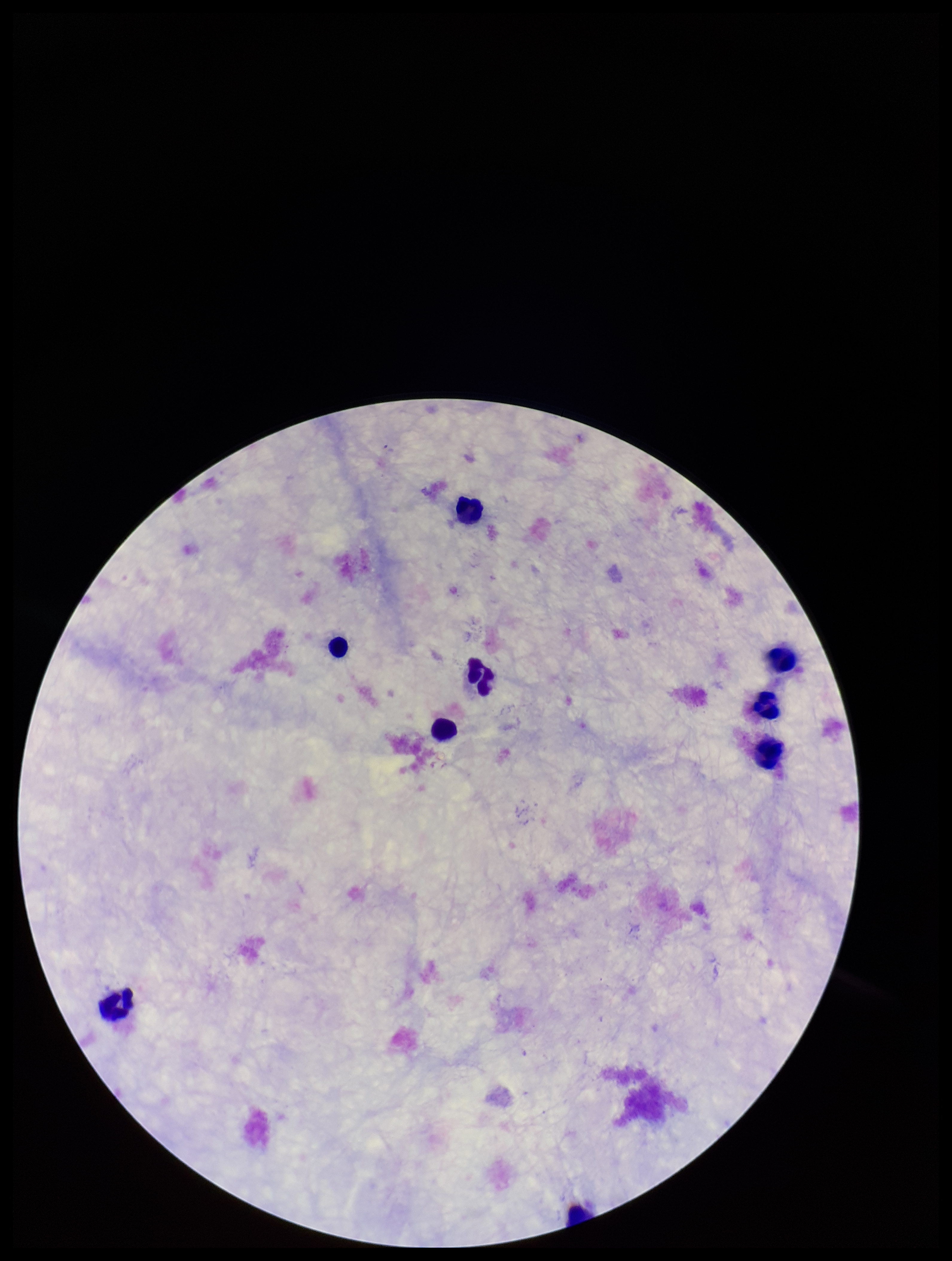

Summary:
  - Image size: 952×1261 pixels
  - Field of view: one from this slide
  - Patient malaria status: negative
  - Stain: Giemsa
  - Capture: smartphone photograph through the microscope eyepiece
  - Parasite count: 0
  - Leukocyte count: 9
  - Preparation: thick blood smear
  - Plasmodium parasites: none detected